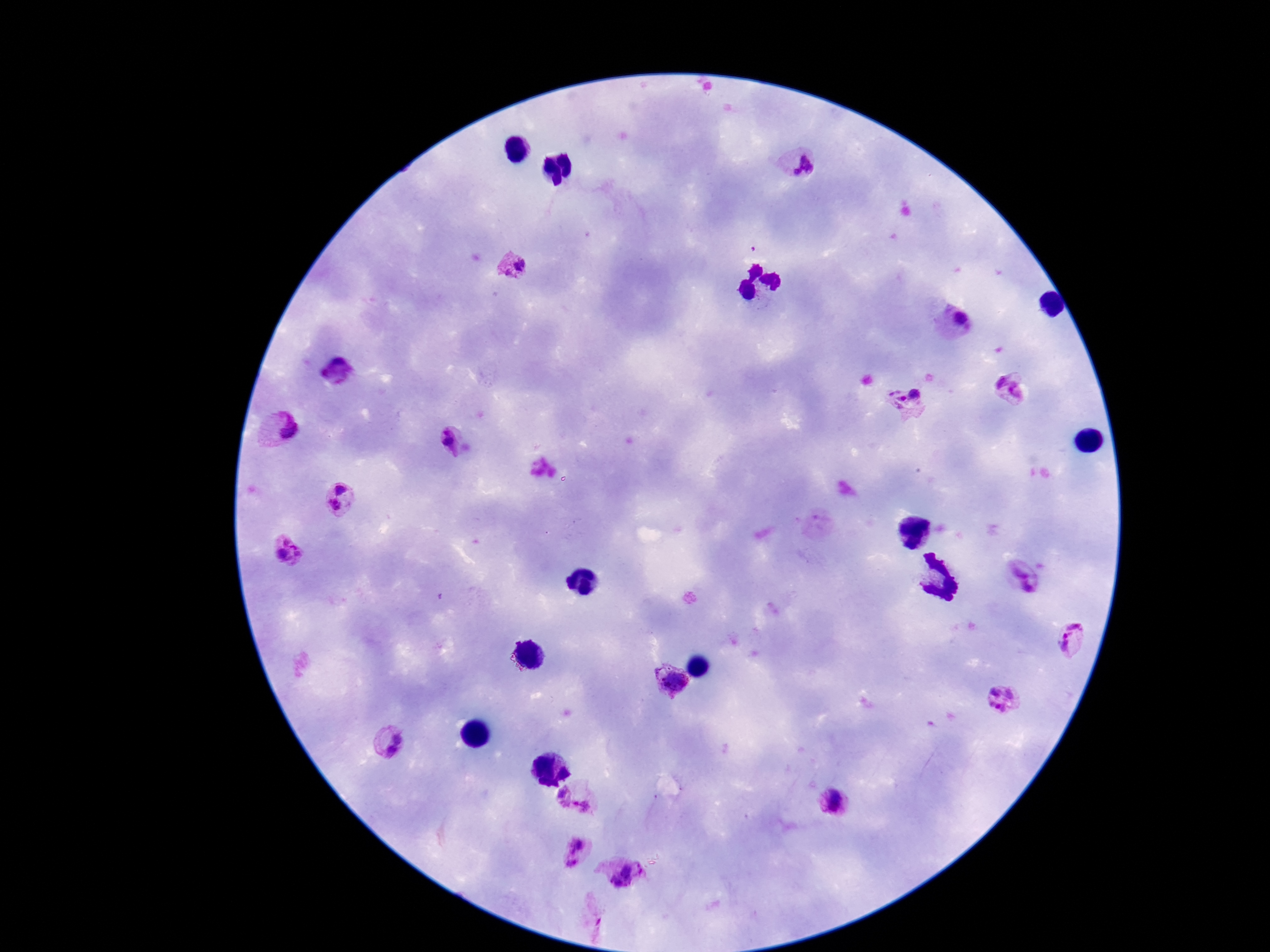

Approximate centers as {x, y} in pixels.
Summary:
  - Plasmodium parasite locations: {803, 166}, {516, 265}, {959, 322}, {1013, 386}, {909, 404}, {279, 431}, {453, 443}, {342, 482}, {332, 508}, {815, 528}, {288, 552}, {1025, 578}, {1074, 640}, {668, 682}, {1003, 700}, {386, 742}, {579, 796}, {831, 803}, {579, 853}, {627, 876}, {592, 920}
  - Patient malaria status: positive
  - Image size: 1270×952 pixels
  - Field of view: one from this slide
  - Stain: Giemsa
  - Capture: smartphone camera through the microscope eyepiece
  - Magnification: 100x
  - Preparation: thick peripheral-blood smear